Identify the parasite.
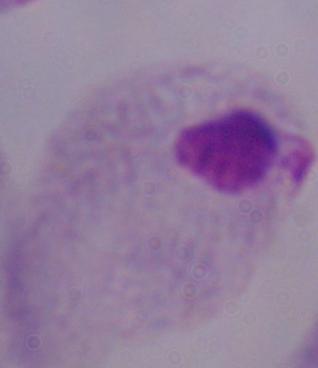
This is a trichomonad.

Photomicrograph. 1000x magnification.